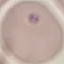

{
  "result": "negative for malaria parasites",
  "capture": "smartphone camera at the microscope eyepiece",
  "image_type": "cell patch, automatically extracted from a larger field of view and resized to 64 × 64 pixels",
  "stain": "Giemsa",
  "preparation": "thin blood film"
}